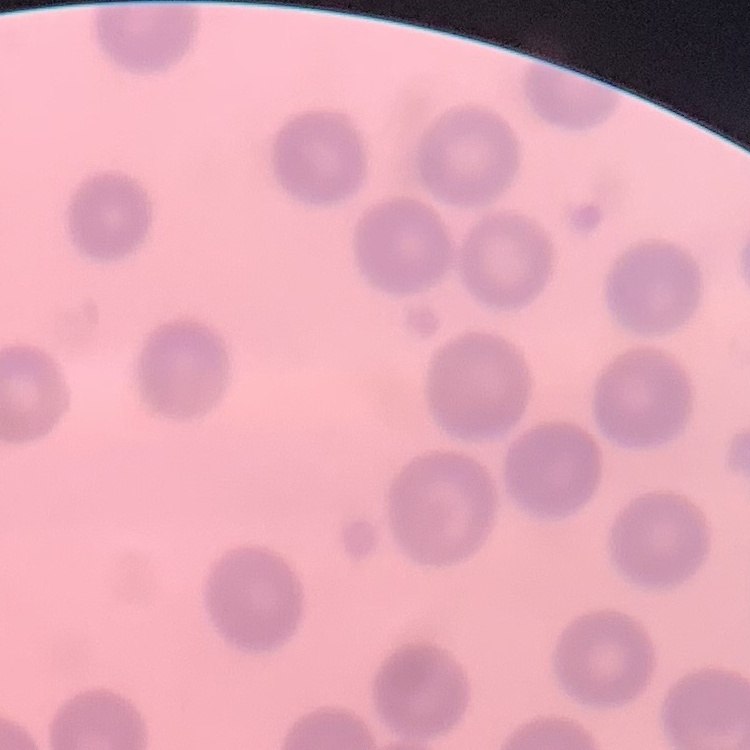 The erythrocytes exhibit no rouleaux formation. Field's or Giemsa stain. Thin blood film. Square crop of a larger photomicrograph.